Locate Plasmodium parasites and leukocytes.
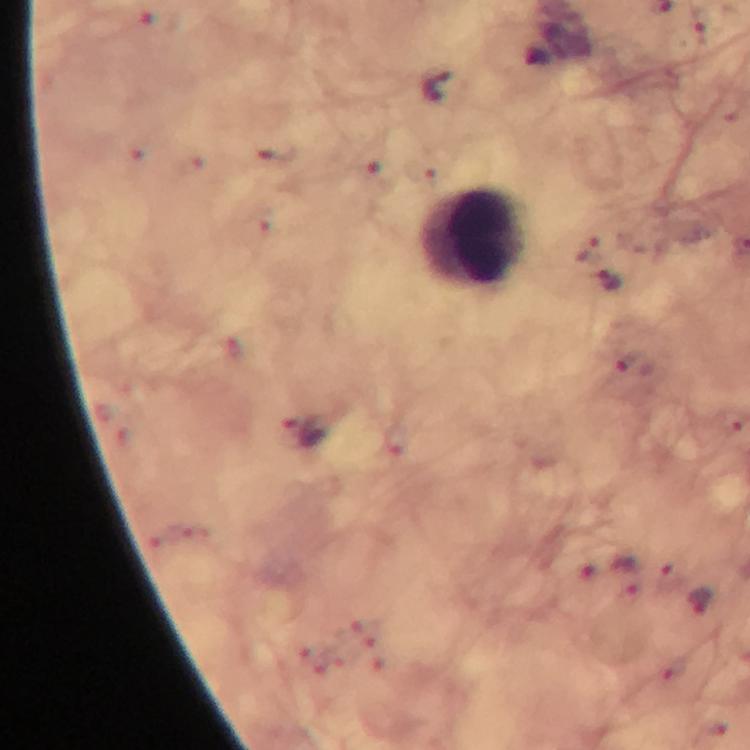

Approximate object centers, in pixels from the top-left corner.
Plasmodium parasites: (x=587, y=247), (x=611, y=282).
Leukocytes: (x=474, y=239).

cropped from = one field of view
image size = 750×750 pixels
capture = smartphone photograph through a microscope
context = from a malaria diagnostic workup
preparation = thick blood film
magnification = 100x
stain = Giemsa
immersion oil = used